Point out each malaria parasite.
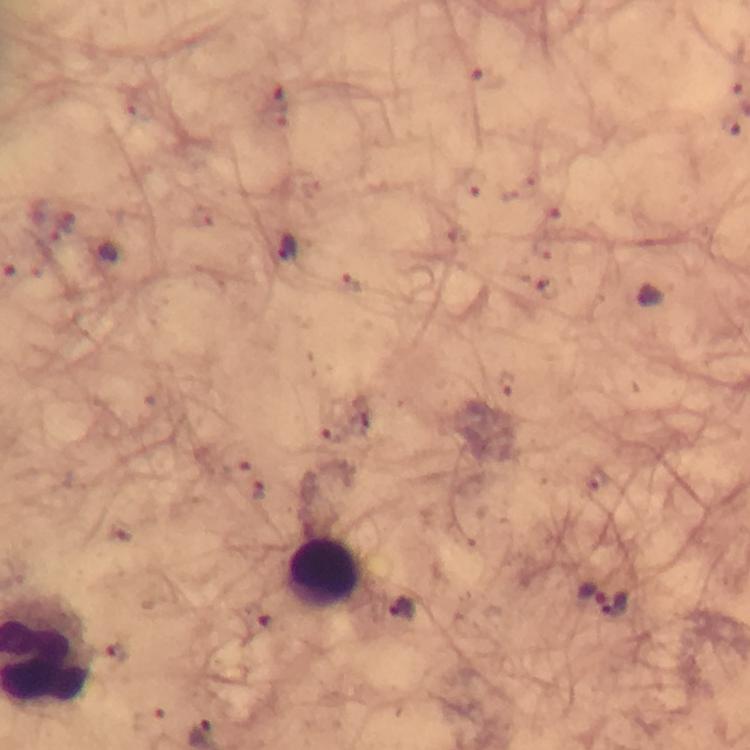
Approximate centers as (x, y) in pixels.
Malaria parasites: (480, 73), (729, 125), (474, 182), (61, 227), (286, 248), (349, 281), (549, 288), (650, 294), (506, 384), (332, 433), (260, 491), (593, 591), (616, 602), (257, 618).

Leukocyte locations: (324, 574). Thick smear. Giemsa stain. Immersion oil applied. Cropped region of a single field of view. Image is 750×750 pixels. Smartphone photograph taken through a microscope. At 100x magnification. From a diagnostic examination for malaria.